Point out Plasmodium parasites and leukocytes.
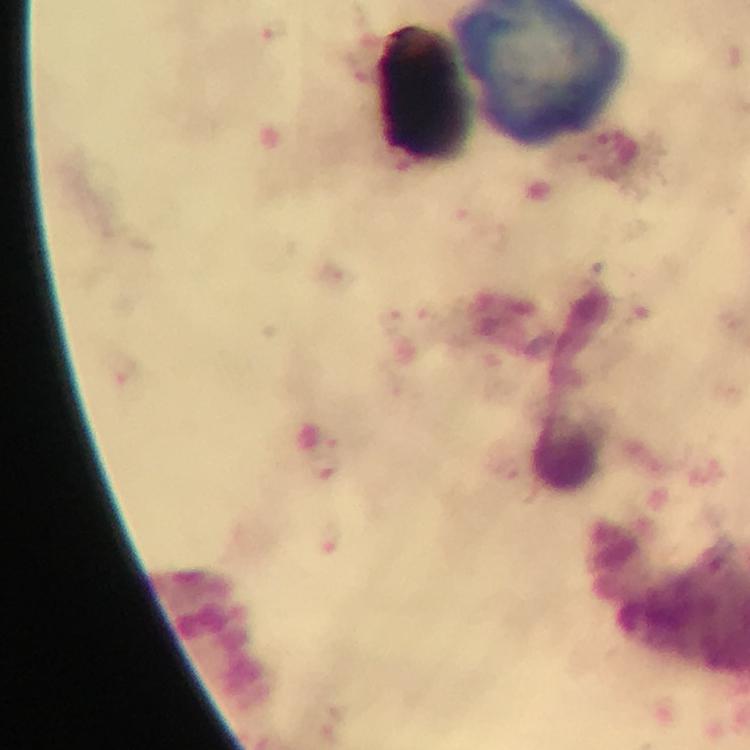

No Plasmodium parasites detected.
Approximate centers as {x, y} in pixels.
Leukocytes: {567, 452}.

Immersion oil applied. From a malaria diagnostic workup. Cropped region of a single field of view. At 100x magnification. Image is 750×750 pixels. Smartphone photograph taken through a microscope. Giemsa stain. Thick smear.